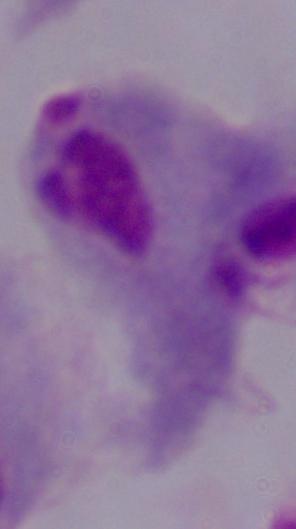
Micrograph. A trichomonad is seen. Captured at 1000x magnification.